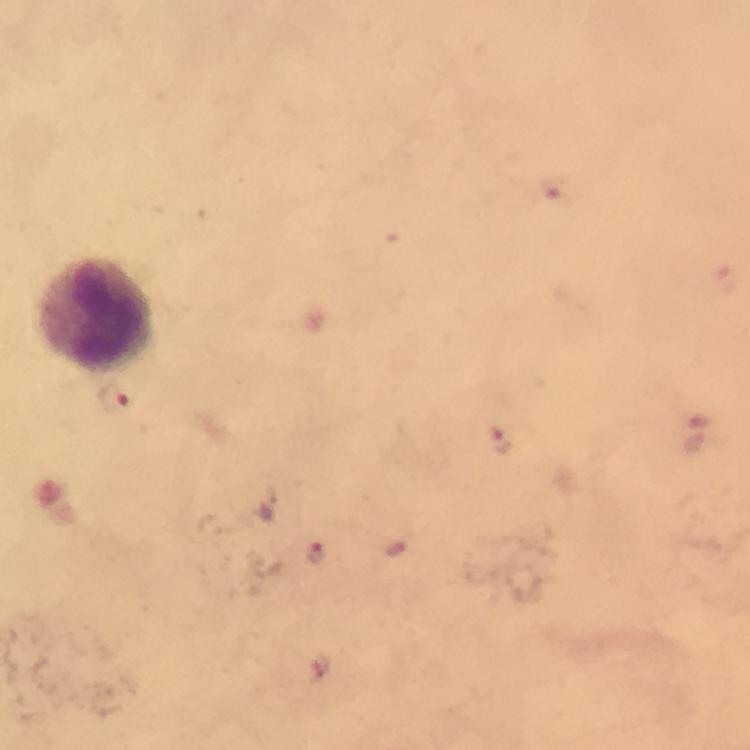
Approximate centers as {x, y} in pixels.
Summary:
  - Leukocyte locations: {101, 317}
  - Malaria parasite locations: {554, 188}, {112, 400}, {502, 442}, {395, 546}, {316, 552}, {321, 668}
  - Capture: smartphone photograph through a microscope
  - Immersion oil: used
  - Magnification: 100x
  - Stain: Giemsa
  - Preparation: thick blood film
  - Image size: 750×750 pixels
  - Cropped from: one field of view
  - Context: from a diagnostic examination for malaria